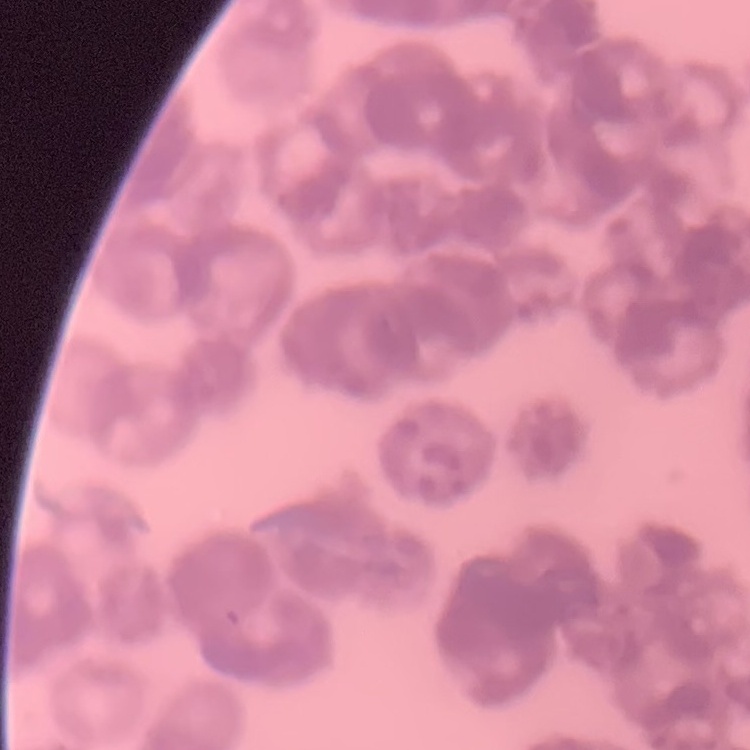
Summary:
  - Red blood cell morphology: rouleaux formation
  - Stain: Field's or Giemsa
  - Image type: one tile cut from a larger photomicrograph
  - Preparation: thin blood film